Outline each Plasmodium ovale-infected red blood cell.
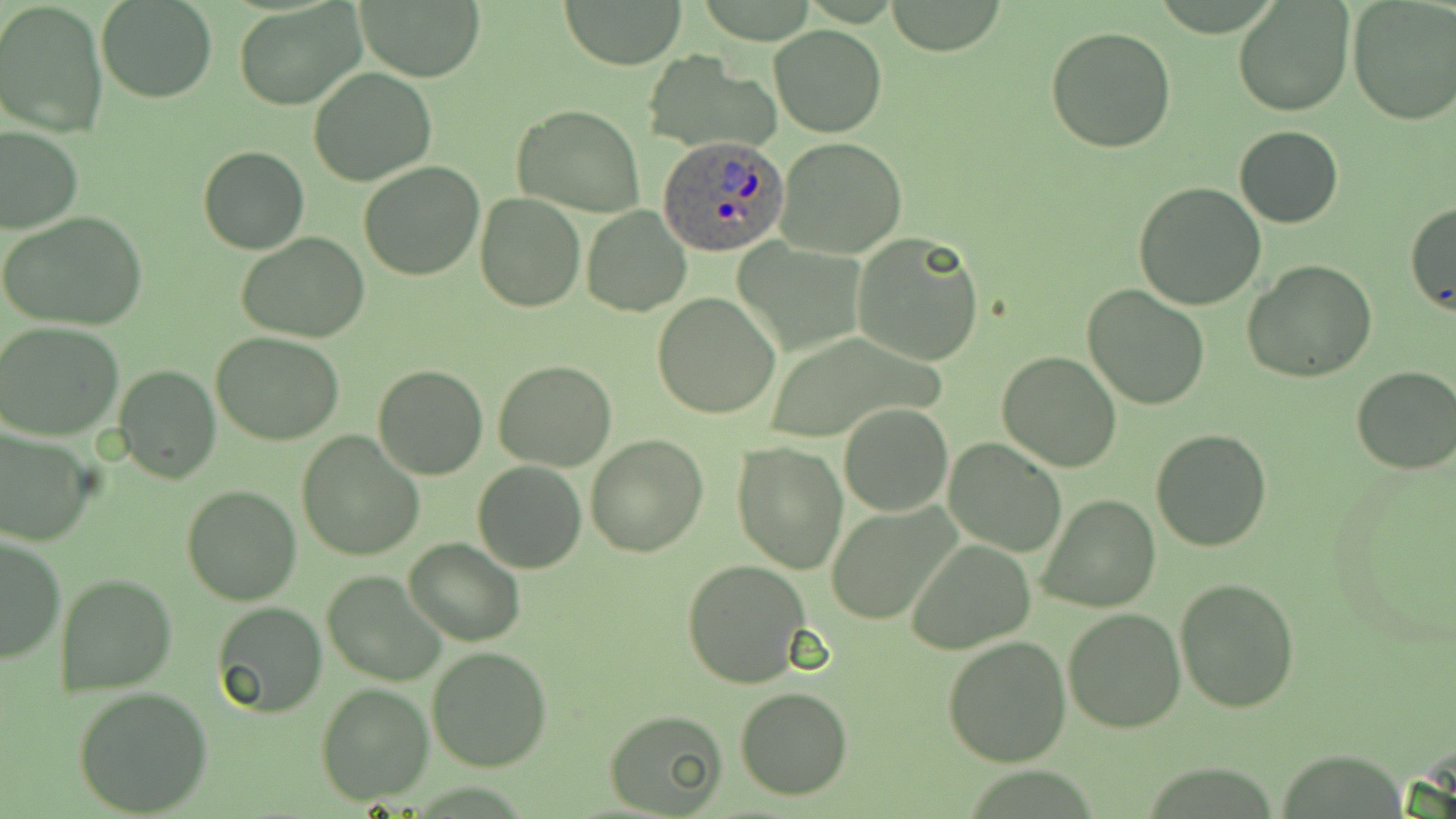
Approximate bounding boxes as named x1/y1/x2/y2 corners in pixels.
Plasmodium ovale-infected red blood cells: (x1=658, y1=132, x2=788, y2=255).

slide-level diagnosis = Plasmodium ovale
image size = 1456×819 pixels
field of view = one of a larger specimen
magnification = 1000x
preparation = thin blood smear
modality = light microscopy
uninfected red blood cell locations = approximate bounding boxes as named x1/y1/x2/y2 corners in pixels: (x1=0, y1=0, x2=109, y2=140), (x1=558, y1=0, x2=689, y2=68), (x1=354, y1=1, x2=484, y2=81), (x1=1233, y1=1, x2=1355, y2=119), (x1=96, y1=2, x2=217, y2=103), (x1=234, y1=2, x2=365, y2=112), (x1=883, y1=2, x2=1007, y2=55), (x1=1347, y1=3, x2=1454, y2=126), (x1=1046, y1=25, x2=1178, y2=153), (x1=770, y1=26, x2=886, y2=137), (x1=309, y1=68, x2=436, y2=186), (x1=513, y1=104, x2=645, y2=217), (x1=1, y1=126, x2=82, y2=232), (x1=1234, y1=126, x2=1345, y2=228), (x1=776, y1=136, x2=907, y2=260), (x1=198, y1=146, x2=307, y2=255), (x1=358, y1=161, x2=487, y2=280), (x1=1132, y1=182, x2=1267, y2=310), (x1=475, y1=191, x2=587, y2=311), (x1=1405, y1=199, x2=1456, y2=313), (x1=581, y1=205, x2=691, y2=317), (x1=1, y1=212, x2=150, y2=332), (x1=851, y1=230, x2=986, y2=366), (x1=237, y1=233, x2=372, y2=344), (x1=1241, y1=260, x2=1378, y2=382), (x1=1083, y1=284, x2=1212, y2=409), (x1=652, y1=293, x2=782, y2=420), (x1=1, y1=323, x2=124, y2=441), (x1=211, y1=331, x2=345, y2=444), (x1=996, y1=351, x2=1122, y2=473), (x1=493, y1=359, x2=617, y2=472), (x1=373, y1=363, x2=489, y2=480), (x1=115, y1=364, x2=220, y2=483), (x1=1350, y1=364, x2=1456, y2=475), (x1=839, y1=402, x2=952, y2=517), (x1=1150, y1=429, x2=1272, y2=551), (x1=0, y1=431, x2=94, y2=548), (x1=295, y1=432, x2=425, y2=561), (x1=585, y1=434, x2=708, y2=556), (x1=945, y1=439, x2=1065, y2=557), (x1=731, y1=440, x2=848, y2=575), (x1=472, y1=461, x2=587, y2=574), (x1=181, y1=484, x2=303, y2=605), (x1=1038, y1=492, x2=1162, y2=612), (x1=828, y1=504, x2=960, y2=626), (x1=0, y1=534, x2=64, y2=665), (x1=404, y1=539, x2=525, y2=647), (x1=906, y1=540, x2=1036, y2=654), (x1=682, y1=558, x2=812, y2=688), (x1=321, y1=570, x2=446, y2=687), (x1=55, y1=573, x2=177, y2=695), (x1=1173, y1=578, x2=1300, y2=714), (x1=211, y1=601, x2=328, y2=717), (x1=1062, y1=607, x2=1185, y2=733), (x1=940, y1=635, x2=1071, y2=768), (x1=427, y1=645, x2=551, y2=772), (x1=316, y1=684, x2=433, y2=806), (x1=73, y1=686, x2=214, y2=816), (x1=735, y1=686, x2=853, y2=801), (x1=604, y1=707, x2=727, y2=816)
stain = May-Grünwald-Giemsa